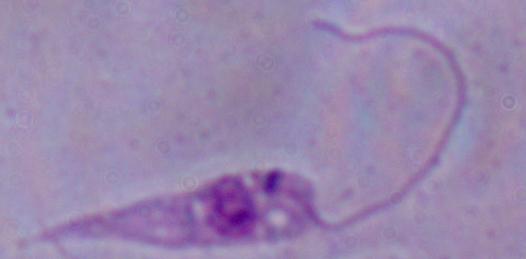

modality = photomicrograph
identification = Leishmania
magnification = 1000x